Classify this cell by malaria status.
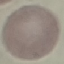
It is uninfected.

Cell patch, automatically extracted from a larger field of view and resized to 64 × 64 pixels. Thin smear of blood. Acquired by smartphone through the microscope eyepiece. Giemsa-stained preparation.